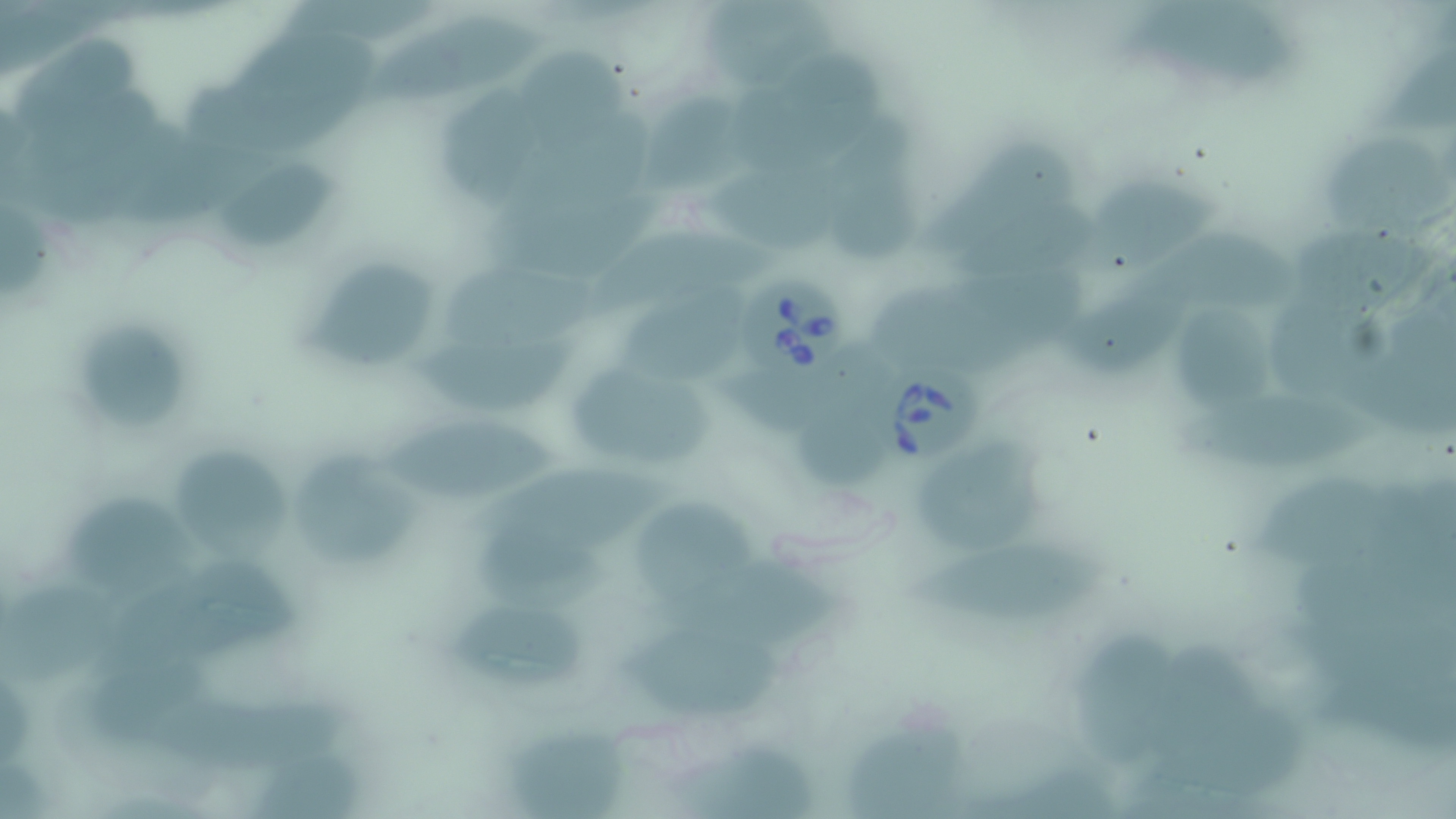 Approximate bounding boxes as (x1,y1)-(x2,y2) corner pairs in pixels. Babesia divergens-infected red blood cell locations: (739,279)-(845,389), (861,355)-(979,465). Uninfected red blood cell locations: (701,1)-(858,91), (1126,2)-(1304,90), (363,16)-(546,109), (240,24)-(383,117), (13,35)-(138,153), (520,50)-(637,157), (725,57)-(892,173), (177,72)-(367,158), (440,82)-(550,212), (639,100)-(752,193), (823,119)-(932,264), (916,139)-(1078,263), (1326,139)-(1452,235), (709,154)-(863,257), (216,161)-(339,244), (1067,177)-(1221,277), (589,221)-(783,318), (1279,225)-(1436,335), (1133,238)-(1302,318), (948,242)-(1098,342), (311,260)-(429,369), (444,264)-(591,358), (1064,277)-(1211,378), (867,283)-(1032,374), (629,287)-(755,386), (1258,296)-(1408,403), (1176,310)-(1275,420), (79,322)-(193,430), (409,336)-(583,418), (719,342)-(897,437), (568,363)-(716,471), (1176,390)-(1386,477), (804,394)-(897,493), (383,421)-(566,508), (913,438)-(1055,556), (177,449)-(286,559), (295,454)-(428,567), (457,462)-(694,560), (1251,465)-(1390,575), (70,493)-(200,597), (633,500)-(761,618), (476,527)-(622,609), (904,543)-(1110,626), (661,555)-(849,657), (1,586)-(123,685), (452,602)-(590,693), (625,623)-(787,719), (1082,633)-(1181,765), (1136,645)-(1280,770), (842,719)-(969,819), (505,721)-(633,819), (677,739)-(824,819), (248,749)-(374,819). Slide-level diagnosis: Babesia divergens. Single field of view. Image is 1456×819 pixels. Captured at 1000x magnification. Thin blood film. Optical microscopy. May-Grünwald-Giemsa stain.